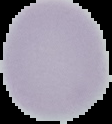

Cell region segmented out of the field of view; the surrounding area is masked to black. Result: no malaria parasites detected. From a thin blood film. Image is 112×124 pixels.